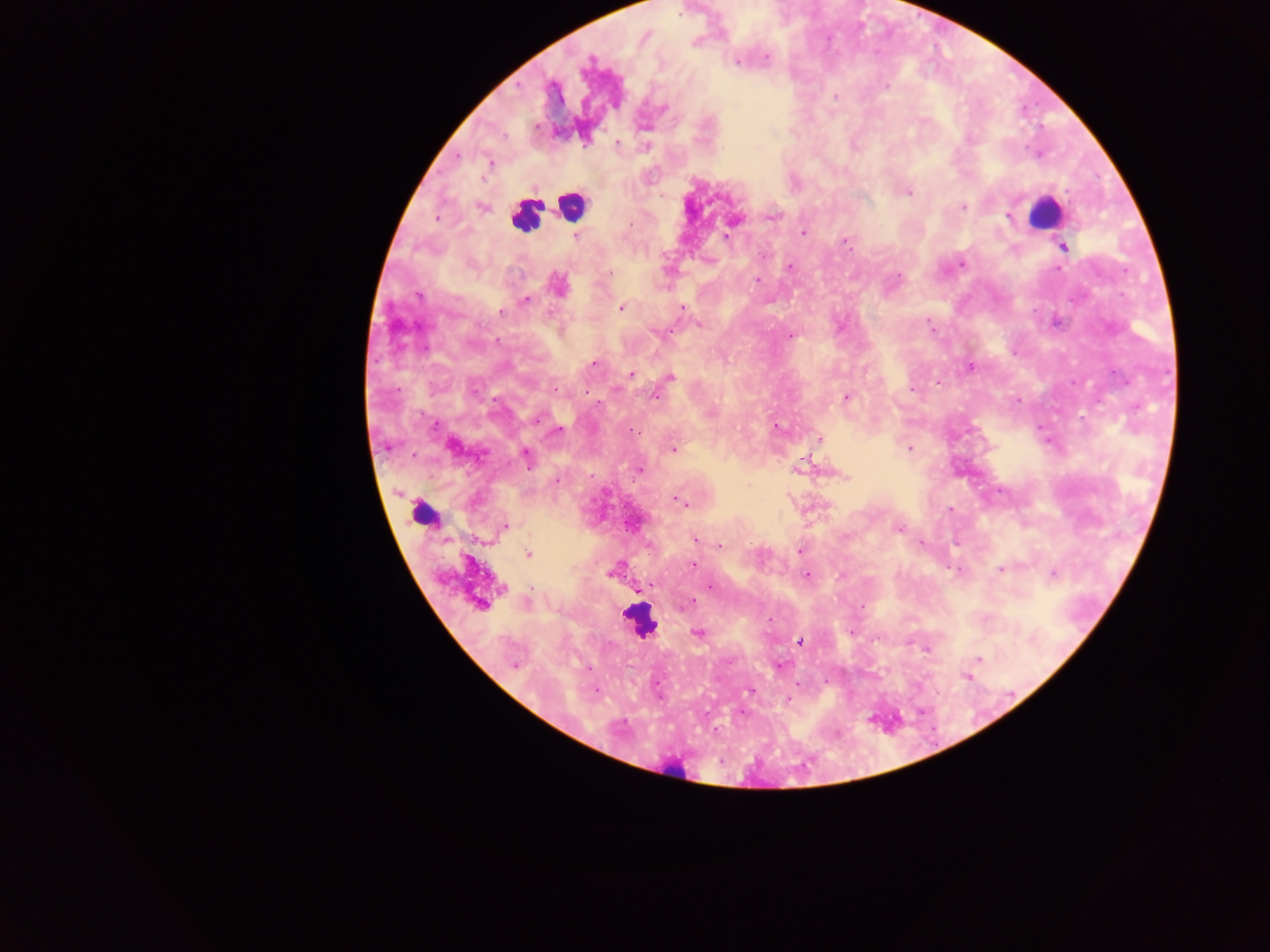
Approximate centers as x y in pixels.
Summary:
  - Plasmodium parasite locations: 766 57; 737 62; 886 86; 836 96; 663 107; 536 126; 970 139; 617 142; 489 163; 908 192; 963 207; 481 208; 773 215; 1009 216; 437 217; 630 224; 803 232; 575 236; 726 236; 846 242; 1063 246; 962 264; 789 267; 1058 269; 899 275; 757 280; 558 284; 418 295; 526 301; 621 308; 683 308; 501 311; 928 321; 699 326; 658 333; 791 336; 594 363; 970 367; 631 374; 670 377; 939 382; 556 389; 912 389; 655 396; 846 397; 1018 401; 538 419; 435 426; 776 427; 558 430; 633 430; 819 439; 452 446; 672 449; 909 449; 526 456; 804 462; 639 470; 846 477; 680 502; 950 509; 504 526; 898 529; 695 540; 720 545; 800 551; 528 554; 692 564; 1001 569; 610 572; 1054 574; 806 575; 711 587; 640 588; 689 603; 480 604; 684 605; 769 619; 698 633; 801 642; 978 659; 515 666; 781 666; 750 692; 788 700
  - Leukocyte locations: 570 206; 1046 212; 526 216; 422 506; 640 621; 672 772
  - Image size: 1270×952 pixels
  - Field of view: single
  - Capture: mobile-phone photograph through a microscope
  - Country: Ghana
  - Preparation: thick blood smear